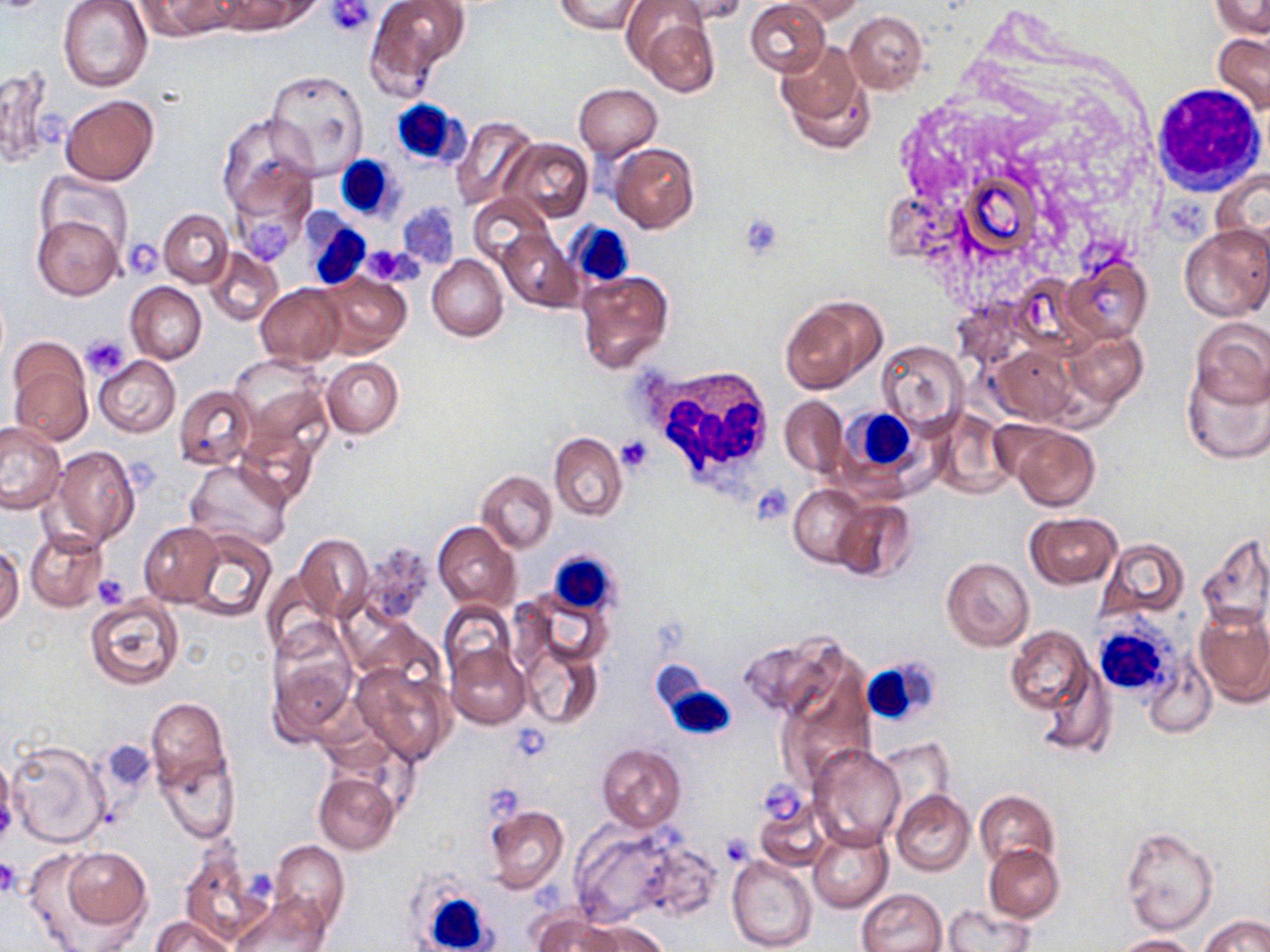
Summary:
  - Coordinate format: approximate bounding boxes as named x1/y1/x2/y2 corners in pixels
  - Platelet locations: (x1=327, y1=1, x2=374, y2=36), (x1=396, y1=207, x2=458, y2=267), (x1=237, y1=208, x2=298, y2=266), (x1=737, y1=213, x2=786, y2=260), (x1=123, y1=238, x2=164, y2=278), (x1=366, y1=246, x2=422, y2=286), (x1=82, y1=335, x2=131, y2=377), (x1=615, y1=436, x2=654, y2=475), (x1=752, y1=485, x2=792, y2=523), (x1=92, y1=572, x2=131, y2=607), (x1=510, y1=726, x2=550, y2=762), (x1=485, y1=785, x2=524, y2=824), (x1=717, y1=834, x2=754, y2=867), (x1=0, y1=856, x2=22, y2=895), (x1=531, y1=884, x2=567, y2=920)
  - White blood cell locations: (x1=1150, y1=79, x2=1268, y2=195), (x1=388, y1=99, x2=468, y2=168), (x1=335, y1=156, x2=399, y2=221), (x1=301, y1=211, x2=371, y2=291), (x1=567, y1=222, x2=634, y2=288), (x1=639, y1=364, x2=770, y2=493), (x1=843, y1=407, x2=919, y2=481), (x1=550, y1=550, x2=620, y2=615), (x1=1091, y1=619, x2=1179, y2=700), (x1=852, y1=650, x2=941, y2=730), (x1=655, y1=672, x2=738, y2=738), (x1=408, y1=878, x2=496, y2=952)
  - Uninfected red blood cell locations: (x1=57, y1=0, x2=152, y2=92), (x1=136, y1=0, x2=233, y2=40), (x1=216, y1=0, x2=317, y2=35), (x1=364, y1=0, x2=469, y2=95), (x1=553, y1=0, x2=643, y2=33), (x1=666, y1=0, x2=751, y2=25), (x1=745, y1=0, x2=830, y2=76), (x1=779, y1=0, x2=866, y2=24), (x1=1209, y1=0, x2=1269, y2=38), (x1=637, y1=12, x2=720, y2=97), (x1=845, y1=12, x2=928, y2=93), (x1=1212, y1=32, x2=1270, y2=117), (x1=776, y1=37, x2=872, y2=153), (x1=0, y1=65, x2=57, y2=167), (x1=265, y1=69, x2=370, y2=177), (x1=573, y1=84, x2=662, y2=159), (x1=60, y1=94, x2=159, y2=185), (x1=214, y1=114, x2=314, y2=224), (x1=451, y1=115, x2=540, y2=212), (x1=502, y1=138, x2=592, y2=223), (x1=610, y1=143, x2=699, y2=232), (x1=951, y1=163, x2=1048, y2=262), (x1=1211, y1=166, x2=1270, y2=261), (x1=37, y1=171, x2=132, y2=253), (x1=468, y1=193, x2=553, y2=268), (x1=159, y1=209, x2=232, y2=286), (x1=32, y1=215, x2=124, y2=300), (x1=1180, y1=222, x2=1270, y2=321), (x1=497, y1=229, x2=580, y2=312), (x1=206, y1=247, x2=284, y2=326), (x1=427, y1=254, x2=508, y2=341), (x1=1060, y1=257, x2=1152, y2=344), (x1=576, y1=271, x2=673, y2=373), (x1=317, y1=273, x2=411, y2=358), (x1=126, y1=282, x2=207, y2=364), (x1=256, y1=284, x2=346, y2=365), (x1=779, y1=294, x2=886, y2=393), (x1=1189, y1=318, x2=1270, y2=408), (x1=1063, y1=330, x2=1147, y2=407), (x1=877, y1=339, x2=970, y2=434), (x1=988, y1=344, x2=1076, y2=424), (x1=7, y1=349, x2=93, y2=446), (x1=229, y1=353, x2=329, y2=440), (x1=94, y1=356, x2=180, y2=437), (x1=321, y1=357, x2=403, y2=438), (x1=1182, y1=363, x2=1270, y2=464), (x1=174, y1=386, x2=257, y2=470), (x1=781, y1=396, x2=847, y2=475), (x1=932, y1=410, x2=1014, y2=498), (x1=0, y1=421, x2=68, y2=514), (x1=999, y1=422, x2=1101, y2=511), (x1=235, y1=428, x2=318, y2=507), (x1=549, y1=433, x2=626, y2=520), (x1=51, y1=445, x2=140, y2=549), (x1=186, y1=461, x2=291, y2=550), (x1=477, y1=471, x2=557, y2=553), (x1=788, y1=485, x2=866, y2=567), (x1=830, y1=497, x2=916, y2=581), (x1=1025, y1=512, x2=1122, y2=589), (x1=433, y1=521, x2=521, y2=612), (x1=139, y1=522, x2=223, y2=606), (x1=25, y1=530, x2=107, y2=612), (x1=183, y1=530, x2=276, y2=622), (x1=1198, y1=532, x2=1270, y2=631), (x1=295, y1=533, x2=374, y2=623), (x1=1097, y1=539, x2=1189, y2=621), (x1=0, y1=546, x2=24, y2=625), (x1=941, y1=557, x2=1035, y2=651), (x1=262, y1=570, x2=341, y2=654), (x1=85, y1=594, x2=184, y2=690), (x1=440, y1=601, x2=516, y2=687), (x1=1194, y1=605, x2=1270, y2=707), (x1=266, y1=624, x2=358, y2=741), (x1=1006, y1=626, x2=1096, y2=717), (x1=737, y1=630, x2=852, y2=723), (x1=519, y1=639, x2=600, y2=729), (x1=446, y1=642, x2=532, y2=729), (x1=1144, y1=656, x2=1216, y2=739), (x1=350, y1=659, x2=455, y2=765), (x1=774, y1=661, x2=878, y2=783), (x1=146, y1=698, x2=230, y2=789), (x1=4, y1=738, x2=111, y2=850), (x1=873, y1=738, x2=956, y2=819), (x1=100, y1=741, x2=156, y2=795), (x1=596, y1=743, x2=686, y2=831), (x1=809, y1=743, x2=906, y2=850), (x1=0, y1=754, x2=18, y2=847), (x1=158, y1=754, x2=238, y2=842), (x1=314, y1=771, x2=399, y2=854), (x1=891, y1=789, x2=974, y2=876), (x1=975, y1=789, x2=1061, y2=872), (x1=753, y1=798, x2=833, y2=873), (x1=484, y1=804, x2=568, y2=893), (x1=568, y1=822, x2=687, y2=926), (x1=808, y1=824, x2=893, y2=913), (x1=1120, y1=827, x2=1217, y2=934), (x1=634, y1=839, x2=722, y2=922), (x1=270, y1=841, x2=349, y2=933), (x1=984, y1=843, x2=1065, y2=922), (x1=61, y1=847, x2=151, y2=929), (x1=180, y1=850, x2=272, y2=948), (x1=727, y1=853, x2=818, y2=951), (x1=857, y1=888, x2=947, y2=952), (x1=230, y1=893, x2=329, y2=952), (x1=940, y1=902, x2=1036, y2=952), (x1=533, y1=914, x2=626, y2=952), (x1=1201, y1=915, x2=1269, y2=952), (x1=151, y1=916, x2=236, y2=952), (x1=578, y1=918, x2=670, y2=952), (x1=1110, y1=933, x2=1198, y2=951)
  - Slide-level diagnosis: negative for blood parasites
  - Preparation: thin blood film
  - Image size: 1270×952 pixels
  - Field of view: single
  - Magnification: 1000x
  - Stain: May-Grünwald-Giemsa
  - Modality: optical microscopy